Give the extent of all Plasmodium falciparum-infected red blood cells.
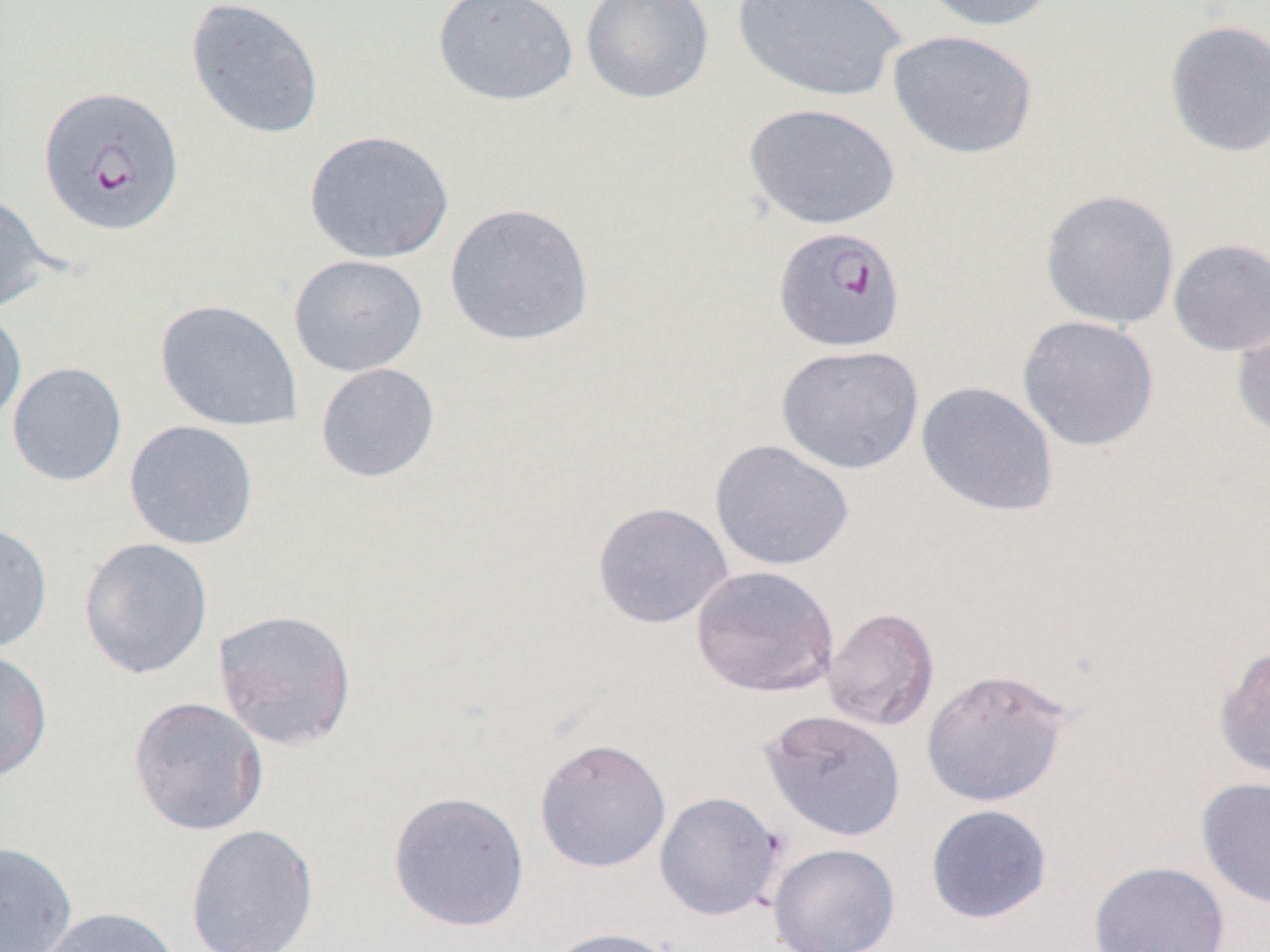

Approximate bounding boxes as (x1,y1)-(x2,y2) corner pairs in pixels.
Plasmodium falciparum-infected red blood cells: (38,85)-(185,237), (772,226)-(906,353).

slide-level diagnosis = Plasmodium falciparum
uninfected red blood cell locations = approximate bounding boxes as (x1,y1)-(x2,y2) corner pairs in pixels: (433,0)-(578,106), (580,0)-(715,104), (732,0)-(906,103), (915,0)-(1063,32), (186,1)-(324,140), (1164,19)-(1270,158), (887,29)-(1039,159), (743,102)-(901,230), (303,130)-(455,264), (1040,188)-(1180,328), (0,192)-(56,314), (444,202)-(595,346), (1168,238)-(1270,355), (288,254)-(428,377), (154,299)-(303,432), (0,304)-(27,429), (1231,310)-(1270,441), (1017,315)-(1160,451), (776,344)-(924,474), (7,361)-(128,487), (315,362)-(440,483), (917,381)-(1059,517), (124,420)-(259,550), (710,439)-(854,572), (592,501)-(733,629), (0,521)-(53,654), (78,537)-(214,680), (690,564)-(839,697), (823,607)-(939,731), (212,608)-(358,751), (1214,644)-(1270,782), (0,648)-(53,782), (920,667)-(1073,807), (128,695)-(269,836), (759,708)-(906,842), (534,737)-(671,873), (1196,777)-(1270,909), (387,790)-(530,932), (654,791)-(785,920), (925,804)-(1053,924), (186,823)-(319,952), (0,840)-(78,952), (768,843)-(900,952), (1088,860)-(1230,952), (34,906)-(183,952), (542,926)-(681,952)
image size = 1270×952 pixels
modality = optical microscopy
field of view = single
preparation = thin blood film
magnification = 1000x